Report the malaria status of this cell.
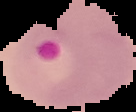
Parasitized.

Summary:
  - Image type: cell region segmented out of the field of view; surrounding area masked to black
  - Preparation: thin blood film
  - Image size: 136×112 pixels